Name the parasite shown.
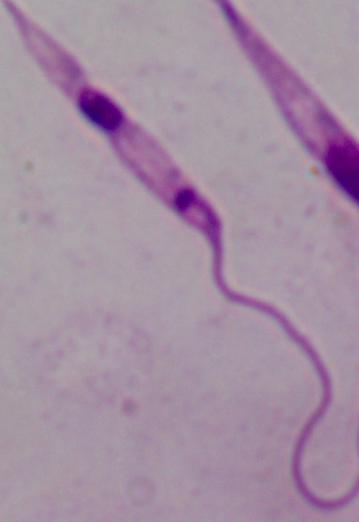
This is Leishmania.

Micrograph. Captured at 1000x magnification.